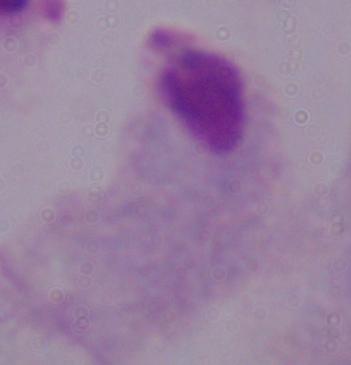
modality: photomicrograph
magnification: 1000x
identification: trichomonad